Assess this cell for malaria.
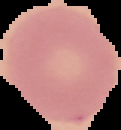
Uninfected.

preparation = thin blood film
image type = cell region segmented out of the field of view; surrounding area masked to black
image size = 121×130 pixels